Classify this cell by malaria status.
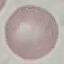

It is uninfected.

stain = Giemsa
image type = automatically extracted cell patch, resized to 64 × 64 pixels
capture = smartphone through the microscope eyepiece
preparation = thin smear